Name the cell type shown.
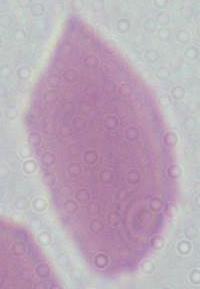
An erythrocyte.

magnification = 1000x
modality = photomicrograph